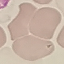

Malaria status: uninfected. Thin smear of blood. Photographed with a smartphone camera at the microscope eyepiece. Giemsa-stained preparation. Cell patch, automatically extracted from a larger field of view and resized to 64 × 64 pixels.